Describe the morphology of the erythrocytes.
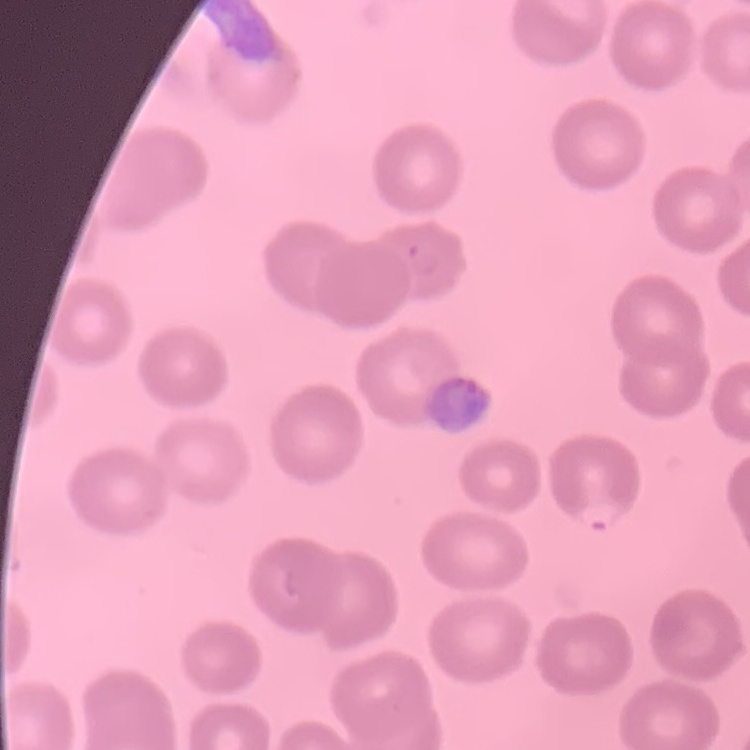

No rouleaux formation.

preparation = thin blood film
stain = Field's or Giemsa
image type = one tile cut from a larger photomicrograph